Locate and identify every blood parasite.
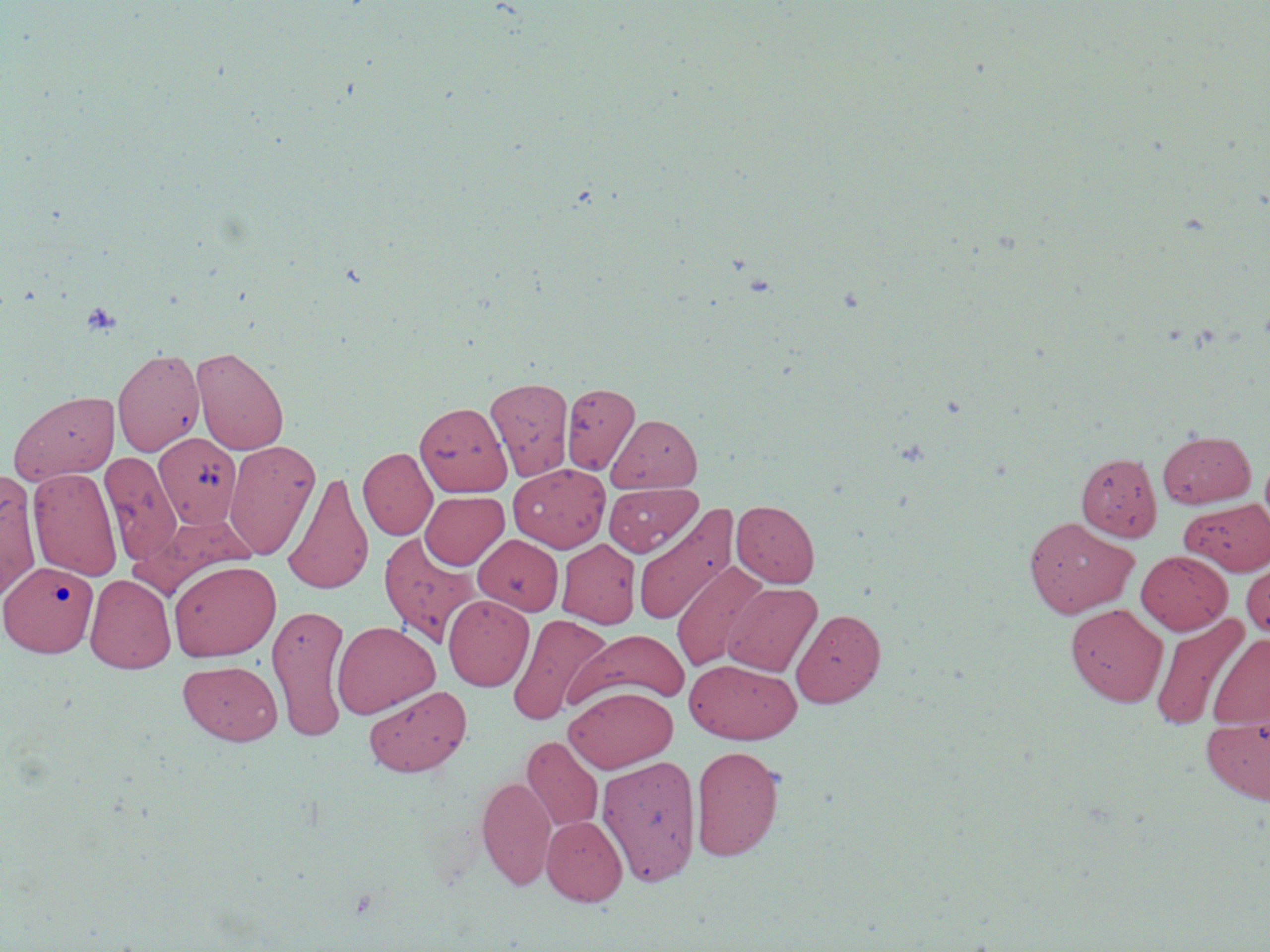

No blood parasites seen.

Approximate bounding boxes as (x1, y1, x2, y2) in pixels. Uninfected red blood cell locations: (192, 346, 289, 455), (112, 348, 205, 456), (485, 377, 574, 481), (561, 382, 639, 474), (8, 389, 119, 485), (415, 401, 512, 497), (607, 413, 702, 493), (1157, 429, 1255, 508), (154, 432, 241, 528), (224, 439, 320, 560), (358, 447, 437, 540), (99, 451, 182, 566), (1076, 451, 1162, 541), (508, 463, 610, 552), (28, 466, 123, 581), (0, 469, 42, 601), (282, 471, 374, 596), (603, 482, 701, 557), (420, 491, 508, 570), (1181, 497, 1270, 575), (731, 500, 819, 587), (633, 504, 738, 627), (1023, 516, 1138, 618), (378, 532, 480, 647), (473, 534, 563, 615), (557, 538, 640, 628), (1136, 550, 1232, 634), (1240, 558, 1270, 639), (1, 560, 98, 657), (169, 560, 280, 661), (671, 560, 768, 672), (85, 573, 176, 673), (723, 582, 822, 676), (443, 595, 534, 691), (267, 603, 350, 741), (1066, 603, 1168, 706), (791, 608, 886, 708), (1150, 611, 1250, 731), (506, 613, 613, 726), (332, 620, 440, 719), (570, 629, 690, 709), (1208, 633, 1270, 729), (684, 658, 801, 744), (178, 660, 282, 745), (363, 685, 472, 777), (564, 685, 679, 773), (1202, 717, 1270, 804), (522, 736, 602, 831), (691, 745, 784, 860), (596, 754, 702, 887), (477, 774, 556, 890), (541, 815, 627, 905). Platelet locations: (81, 301, 122, 336). Slide-level diagnosis: no evidence of blood parasites. Thin blood film. Image is 1270×952 pixels. Optical microscopy. 1000x magnification. May-Grünwald-Giemsa-stained preparation. One field of a larger specimen.